Identify the parasite.
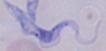

A trypanosome.

Micrograph. Captured at 1000x magnification.